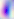

Summary:
  - Magnification: 400x
  - Modality: photomicrograph
  - Identification: Toxoplasma gondii